Name the parasite shown.
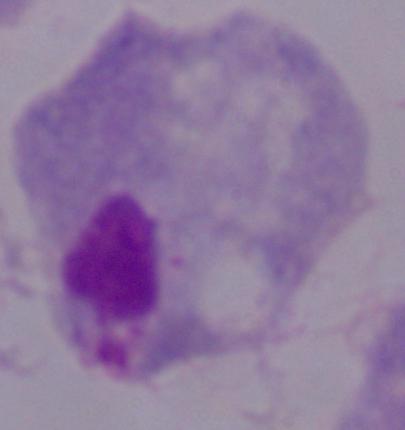
A trichomonad.

modality = micrograph
magnification = 1000x